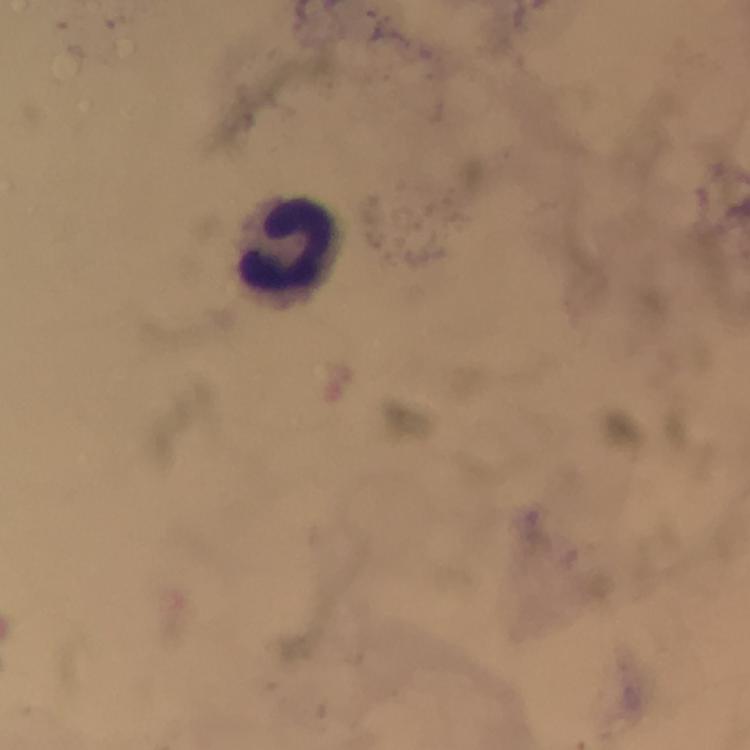

stain = Giemsa
context = from a malaria diagnostic workup
image size = 750×750 pixels
cropped from = one field of view
capture = smartphone camera through the microscope
preparation = thick blood film
magnification = 100x
immersion oil = applied
malaria parasites = none detected
leukocyte locations = approximate centers as (x, y) in pixels: (284, 243)